Name the blood parasite species.
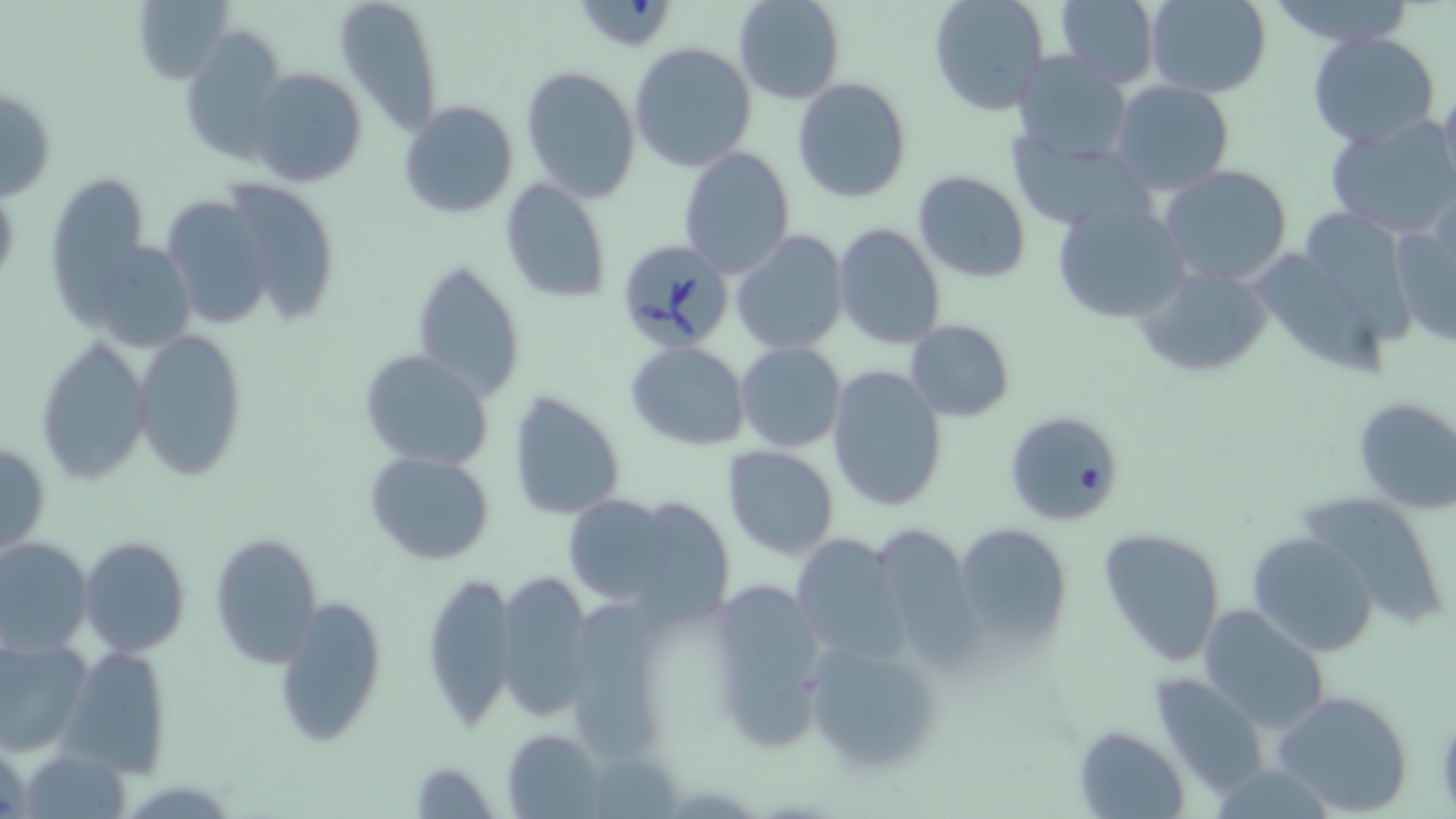

Babesia divergens.

Approximate bounding boxes as named x1/y1/x2/y2 corners in pixels. Uninfected red blood cell locations: (x1=132, y1=0, x2=235, y2=84), (x1=334, y1=0, x2=445, y2=134), (x1=732, y1=0, x2=844, y2=104), (x1=926, y1=0, x2=1051, y2=117), (x1=1145, y1=0, x2=1273, y2=98), (x1=574, y1=1, x2=682, y2=56), (x1=1051, y1=1, x2=1160, y2=87), (x1=181, y1=28, x2=289, y2=162), (x1=1307, y1=33, x2=1439, y2=148), (x1=629, y1=42, x2=757, y2=175), (x1=1011, y1=52, x2=1134, y2=162), (x1=245, y1=66, x2=368, y2=189), (x1=519, y1=66, x2=642, y2=200), (x1=1438, y1=75, x2=1456, y2=203), (x1=792, y1=78, x2=912, y2=204), (x1=1109, y1=81, x2=1236, y2=197), (x1=1, y1=84, x2=55, y2=202), (x1=398, y1=100, x2=518, y2=219), (x1=1324, y1=114, x2=1456, y2=238), (x1=1006, y1=132, x2=1149, y2=230), (x1=678, y1=148, x2=795, y2=279), (x1=1158, y1=163, x2=1293, y2=287), (x1=911, y1=169, x2=1032, y2=284), (x1=46, y1=173, x2=147, y2=317), (x1=221, y1=179, x2=340, y2=323), (x1=498, y1=179, x2=612, y2=303), (x1=159, y1=195, x2=275, y2=331), (x1=1303, y1=197, x2=1413, y2=359), (x1=1052, y1=198, x2=1188, y2=325), (x1=1389, y1=211, x2=1456, y2=348), (x1=833, y1=223, x2=945, y2=350), (x1=730, y1=231, x2=849, y2=355), (x1=102, y1=246, x2=200, y2=349), (x1=1257, y1=248, x2=1386, y2=381), (x1=410, y1=258, x2=526, y2=402), (x1=1132, y1=260, x2=1277, y2=381), (x1=904, y1=320, x2=1015, y2=421), (x1=132, y1=327, x2=247, y2=480), (x1=36, y1=337, x2=151, y2=484), (x1=625, y1=341, x2=749, y2=450), (x1=735, y1=342, x2=845, y2=453), (x1=358, y1=348, x2=494, y2=472), (x1=826, y1=364, x2=948, y2=512), (x1=506, y1=391, x2=628, y2=521), (x1=1350, y1=397, x2=1456, y2=516), (x1=1008, y1=418, x2=1118, y2=522), (x1=0, y1=439, x2=49, y2=560), (x1=722, y1=445, x2=841, y2=560), (x1=363, y1=451, x2=496, y2=566), (x1=1298, y1=492, x2=1451, y2=628), (x1=560, y1=495, x2=680, y2=606), (x1=627, y1=497, x2=733, y2=625), (x1=865, y1=521, x2=980, y2=661), (x1=953, y1=523, x2=1072, y2=647), (x1=1096, y1=525, x2=1227, y2=667), (x1=789, y1=532, x2=909, y2=665), (x1=1246, y1=532, x2=1376, y2=659), (x1=210, y1=533, x2=323, y2=667), (x1=79, y1=536, x2=190, y2=656), (x1=0, y1=537, x2=92, y2=657), (x1=495, y1=566, x2=596, y2=724), (x1=419, y1=569, x2=518, y2=730), (x1=707, y1=575, x2=833, y2=754), (x1=271, y1=597, x2=388, y2=746), (x1=574, y1=604, x2=672, y2=759), (x1=1197, y1=604, x2=1331, y2=735), (x1=0, y1=634, x2=93, y2=756), (x1=803, y1=637, x2=944, y2=775), (x1=58, y1=643, x2=172, y2=777), (x1=1149, y1=672, x2=1271, y2=796), (x1=1270, y1=688, x2=1414, y2=816), (x1=1075, y1=726, x2=1191, y2=817), (x1=501, y1=728, x2=607, y2=817), (x1=0, y1=735, x2=31, y2=819), (x1=409, y1=759, x2=499, y2=818). Babesia divergens-infected red blood cell locations: (x1=612, y1=239, x2=738, y2=352). Image is 1456×819 pixels. Captured at 1000x magnification. Light microscopy. May-Grünwald-Giemsa stain. Single field of view. Thin blood smear.